Comment on the morphology of the erythrocytes.
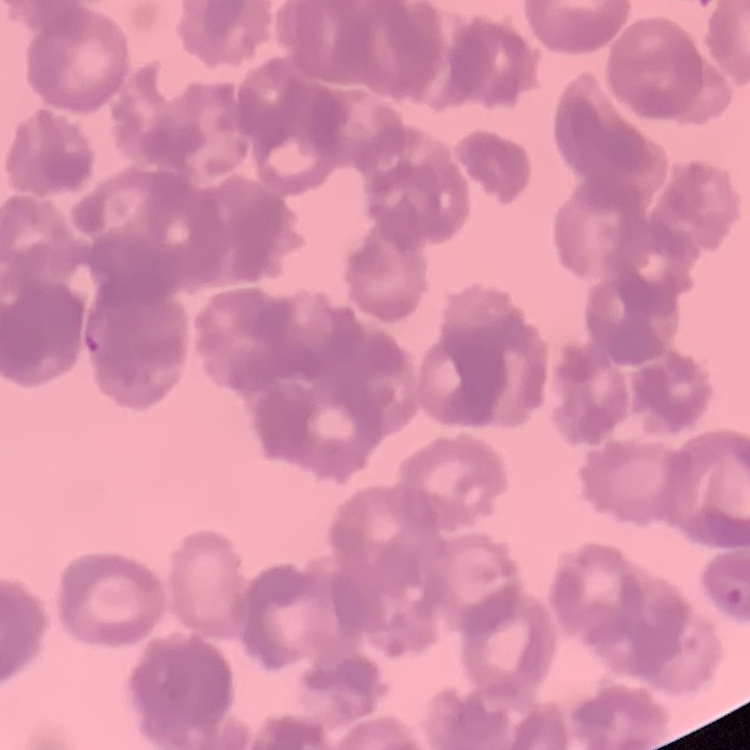
Rouleaux formation.

Summary:
  - Image type: square crop of a larger photomicrograph
  - Preparation: thin peripheral smear
  - Stain: Field's or Giemsa